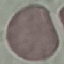
malaria status = uninfected
stain = Giemsa
image type = automatically extracted cell patch, resized to 64 × 64 pixels
preparation = thin smear
capture = smartphone camera at the microscope eyepiece